Report the malaria status of this cell.
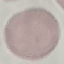

Uninfected.

capture: smartphone camera at the microscope eyepiece
preparation: thin blood smear
image_type: automatically extracted cell patch, resized to 64 × 64 pixels
stain: Giemsa